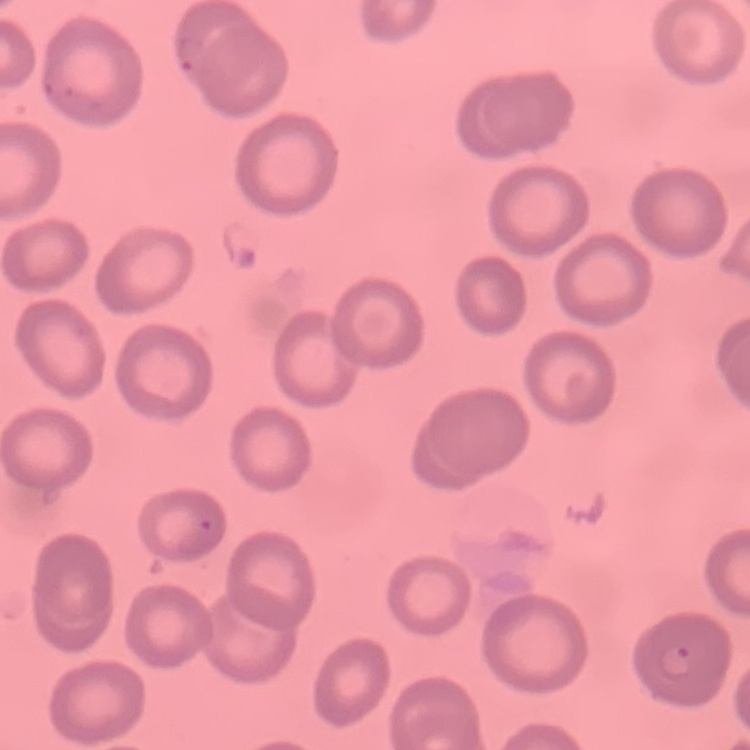
The red blood cells exhibit no rouleaux formation. Field's or Giemsa stain. Square crop of a larger photomicrograph. Thin blood smear.